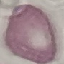
Summary:
  - Result: negative for malaria parasites
  - Capture: smartphone through the microscope eyepiece
  - Preparation: thin blood film
  - Image type: cell patch, automatically extracted from a larger field of view and resized to 64 × 64 pixels
  - Stain: Giemsa